State the blood parasite species.
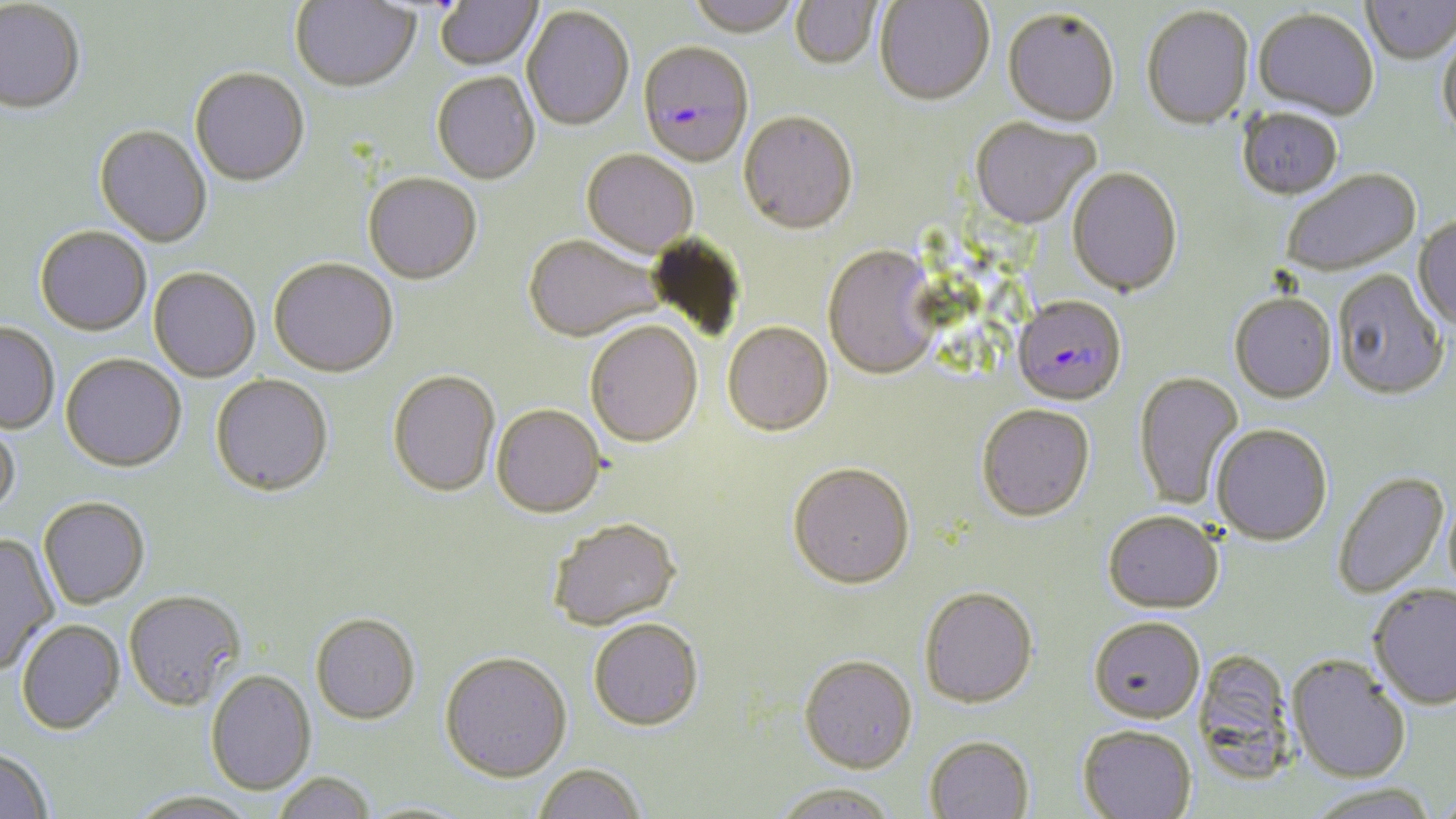

Plasmodium falciparum.

field of view = one of a larger specimen
Plasmodium falciparum-infected red blood cell locations = approximate bounding boxes as named x1/y1/x2/y2 corners in pixels: (x1=637, y1=44, x2=755, y2=170), (x1=1011, y1=296, x2=1127, y2=407)
uninfected red blood cell locations = approximate bounding boxes as named x1/y1/x2/y2 corners in pixels: (x1=435, y1=0, x2=543, y2=73), (x1=686, y1=0, x2=799, y2=40), (x1=0, y1=1, x2=86, y2=116), (x1=291, y1=1, x2=421, y2=94), (x1=790, y1=1, x2=882, y2=72), (x1=875, y1=1, x2=994, y2=108), (x1=1361, y1=1, x2=1456, y2=66), (x1=521, y1=8, x2=634, y2=133), (x1=1141, y1=8, x2=1254, y2=132), (x1=1252, y1=10, x2=1378, y2=123), (x1=1001, y1=11, x2=1120, y2=130), (x1=1437, y1=30, x2=1456, y2=142), (x1=190, y1=70, x2=310, y2=190), (x1=431, y1=73, x2=540, y2=186), (x1=1237, y1=108, x2=1343, y2=203), (x1=738, y1=114, x2=858, y2=238), (x1=970, y1=119, x2=1100, y2=231), (x1=93, y1=126, x2=212, y2=249), (x1=581, y1=151, x2=698, y2=260), (x1=1067, y1=169, x2=1183, y2=299), (x1=1282, y1=170, x2=1422, y2=279), (x1=363, y1=175, x2=482, y2=286), (x1=1412, y1=216, x2=1456, y2=334), (x1=35, y1=227, x2=152, y2=337), (x1=523, y1=236, x2=664, y2=344), (x1=822, y1=246, x2=941, y2=382), (x1=268, y1=260, x2=398, y2=379), (x1=148, y1=269, x2=261, y2=383), (x1=1333, y1=271, x2=1448, y2=402), (x1=1229, y1=294, x2=1337, y2=405), (x1=0, y1=322, x2=59, y2=435), (x1=586, y1=322, x2=703, y2=450), (x1=722, y1=323, x2=833, y2=438), (x1=60, y1=354, x2=186, y2=474), (x1=387, y1=371, x2=500, y2=498), (x1=1133, y1=371, x2=1244, y2=511), (x1=210, y1=375, x2=333, y2=497), (x1=976, y1=404, x2=1095, y2=523), (x1=491, y1=405, x2=606, y2=519), (x1=0, y1=415, x2=21, y2=517), (x1=1210, y1=425, x2=1333, y2=545), (x1=788, y1=464, x2=915, y2=590), (x1=1332, y1=471, x2=1450, y2=599), (x1=38, y1=496, x2=150, y2=608), (x1=1103, y1=511, x2=1223, y2=614), (x1=548, y1=518, x2=681, y2=631), (x1=0, y1=535, x2=59, y2=673), (x1=1368, y1=585, x2=1456, y2=710), (x1=918, y1=587, x2=1039, y2=710), (x1=123, y1=589, x2=246, y2=710), (x1=310, y1=613, x2=421, y2=724), (x1=1088, y1=616, x2=1205, y2=724), (x1=589, y1=618, x2=704, y2=731), (x1=16, y1=619, x2=125, y2=734), (x1=1192, y1=649, x2=1298, y2=780), (x1=440, y1=651, x2=572, y2=781), (x1=799, y1=654, x2=918, y2=773), (x1=1287, y1=654, x2=1411, y2=782), (x1=205, y1=669, x2=316, y2=795), (x1=1077, y1=724, x2=1197, y2=819), (x1=923, y1=735, x2=1035, y2=818), (x1=0, y1=748, x2=53, y2=819), (x1=532, y1=762, x2=645, y2=819), (x1=274, y1=771, x2=376, y2=819), (x1=771, y1=782, x2=899, y2=819), (x1=1306, y1=783, x2=1440, y2=819), (x1=128, y1=790, x2=257, y2=819), (x1=357, y1=800, x2=475, y2=818)
preparation = thin blood film
image size = 1456×819 pixels
stain = May-Grünwald-Giemsa
magnification = 1000x
modality = optical microscopy